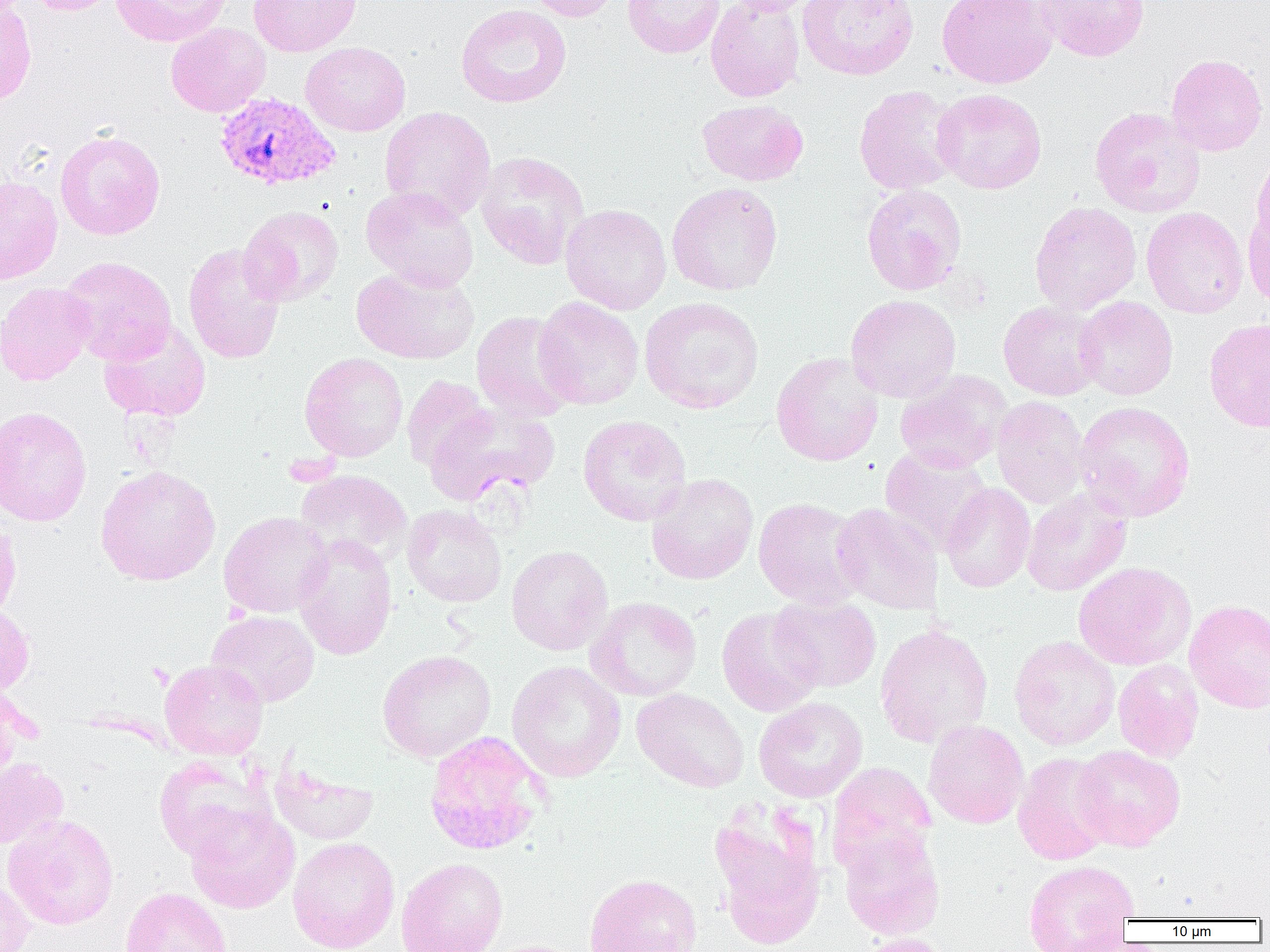

Plasmodium vivax-infected red blood cell locations = approximate bounding boxes as named x1/y1/x2/y2 corners in pixels: (x1=213, y1=91, x2=341, y2=191)
slide-level diagnosis = Plasmodium vivax
magnification = 1000x
preparation = thin blood smear
modality = optical microscopy
image size = 1270×952 pixels
field of view = one of a larger specimen
uninfected red blood cell locations = approximate bounding boxes as named x1/y1/x2/y2 corners in pixels: (x1=22, y1=0, x2=121, y2=15), (x1=111, y1=0, x2=233, y2=47), (x1=248, y1=0, x2=361, y2=57), (x1=523, y1=0, x2=623, y2=22), (x1=622, y1=0, x2=725, y2=59), (x1=705, y1=0, x2=806, y2=102), (x1=721, y1=0, x2=824, y2=16), (x1=798, y1=0, x2=920, y2=80), (x1=937, y1=0, x2=1056, y2=89), (x1=1034, y1=0, x2=1150, y2=62), (x1=0, y1=1, x2=37, y2=109), (x1=455, y1=4, x2=572, y2=108), (x1=165, y1=22, x2=271, y2=117), (x1=300, y1=42, x2=412, y2=136), (x1=1165, y1=54, x2=1267, y2=156), (x1=853, y1=85, x2=963, y2=195), (x1=932, y1=88, x2=1047, y2=194), (x1=697, y1=99, x2=808, y2=186), (x1=1089, y1=106, x2=1206, y2=218), (x1=379, y1=107, x2=496, y2=221), (x1=55, y1=129, x2=166, y2=241), (x1=1250, y1=149, x2=1270, y2=253), (x1=475, y1=151, x2=590, y2=270), (x1=0, y1=175, x2=63, y2=285), (x1=666, y1=182, x2=783, y2=296), (x1=861, y1=184, x2=967, y2=295), (x1=360, y1=186, x2=480, y2=292), (x1=1029, y1=201, x2=1142, y2=315), (x1=560, y1=203, x2=672, y2=314), (x1=1243, y1=204, x2=1270, y2=312), (x1=239, y1=206, x2=344, y2=306), (x1=1141, y1=207, x2=1248, y2=318), (x1=183, y1=243, x2=286, y2=364), (x1=58, y1=256, x2=177, y2=364), (x1=352, y1=266, x2=479, y2=364), (x1=0, y1=282, x2=95, y2=385), (x1=846, y1=294, x2=961, y2=403), (x1=533, y1=296, x2=644, y2=409), (x1=1074, y1=296, x2=1178, y2=400), (x1=640, y1=297, x2=764, y2=414), (x1=998, y1=301, x2=1105, y2=401), (x1=471, y1=310, x2=579, y2=423), (x1=1204, y1=318, x2=1270, y2=433), (x1=98, y1=320, x2=211, y2=422), (x1=299, y1=352, x2=408, y2=462), (x1=771, y1=352, x2=883, y2=466), (x1=894, y1=370, x2=1011, y2=473), (x1=401, y1=375, x2=493, y2=471), (x1=991, y1=396, x2=1090, y2=509), (x1=1074, y1=401, x2=1196, y2=522), (x1=426, y1=402, x2=559, y2=506), (x1=0, y1=405, x2=92, y2=527), (x1=577, y1=414, x2=692, y2=527), (x1=879, y1=445, x2=992, y2=555), (x1=95, y1=465, x2=220, y2=585), (x1=295, y1=470, x2=413, y2=569), (x1=646, y1=473, x2=759, y2=585), (x1=940, y1=483, x2=1036, y2=593), (x1=1022, y1=488, x2=1132, y2=596), (x1=753, y1=497, x2=866, y2=608), (x1=831, y1=503, x2=943, y2=615), (x1=403, y1=504, x2=507, y2=607), (x1=219, y1=511, x2=333, y2=618), (x1=0, y1=517, x2=21, y2=626), (x1=292, y1=535, x2=398, y2=660), (x1=506, y1=545, x2=613, y2=655), (x1=1073, y1=562, x2=1195, y2=670), (x1=769, y1=594, x2=881, y2=692), (x1=586, y1=597, x2=702, y2=701), (x1=1184, y1=599, x2=1270, y2=714), (x1=0, y1=604, x2=34, y2=699), (x1=716, y1=606, x2=824, y2=717), (x1=206, y1=610, x2=320, y2=707), (x1=875, y1=624, x2=993, y2=748), (x1=1009, y1=635, x2=1121, y2=750), (x1=376, y1=650, x2=496, y2=763), (x1=159, y1=659, x2=268, y2=760), (x1=1113, y1=659, x2=1204, y2=763), (x1=506, y1=661, x2=626, y2=782), (x1=631, y1=687, x2=750, y2=793), (x1=0, y1=690, x2=22, y2=787), (x1=753, y1=696, x2=868, y2=802), (x1=923, y1=719, x2=1028, y2=829), (x1=424, y1=731, x2=550, y2=856), (x1=1072, y1=744, x2=1185, y2=850), (x1=1013, y1=752, x2=1116, y2=865), (x1=0, y1=757, x2=68, y2=849), (x1=153, y1=757, x2=275, y2=862), (x1=269, y1=760, x2=378, y2=845), (x1=828, y1=762, x2=936, y2=873), (x1=707, y1=799, x2=827, y2=950), (x1=185, y1=807, x2=300, y2=913), (x1=3, y1=814, x2=119, y2=930), (x1=838, y1=827, x2=945, y2=941), (x1=287, y1=836, x2=400, y2=952), (x1=396, y1=857, x2=507, y2=952), (x1=1023, y1=859, x2=1139, y2=950), (x1=583, y1=873, x2=702, y2=952), (x1=0, y1=876, x2=35, y2=952), (x1=120, y1=886, x2=232, y2=952), (x1=851, y1=934, x2=955, y2=952), (x1=480, y1=939, x2=588, y2=952)